Describe the morphology of the erythrocytes.
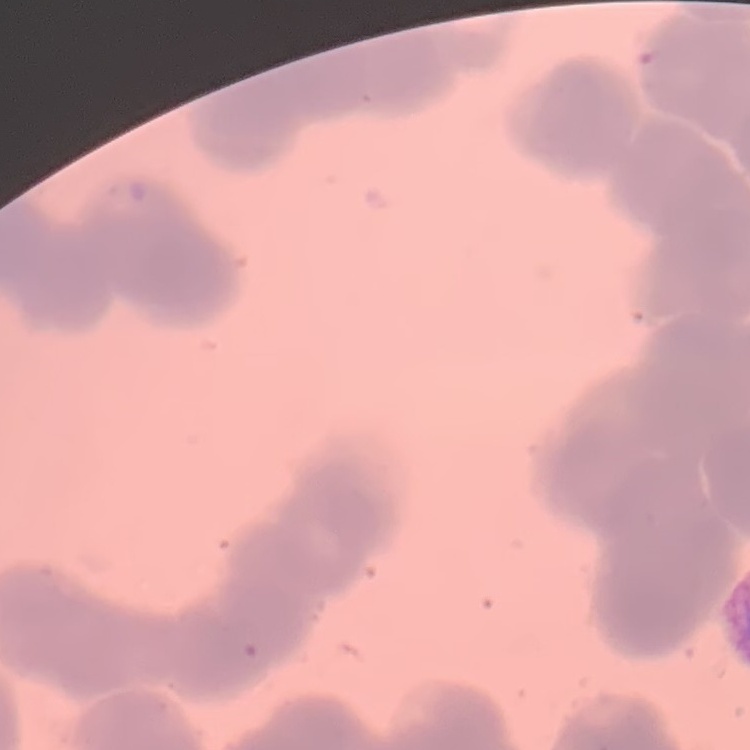
Rouleaux formation.

Summary:
  - Image type: square crop of a larger photomicrograph
  - Preparation: thin blood film
  - Stain: Field's or Giemsa